Assess this cell for malaria.
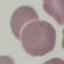
Uninfected.

Thin blood smear. Automatically extracted cell patch, resized to 64 × 64 pixels. Acquired by smartphone through the microscope eyepiece. Giemsa-stained preparation.